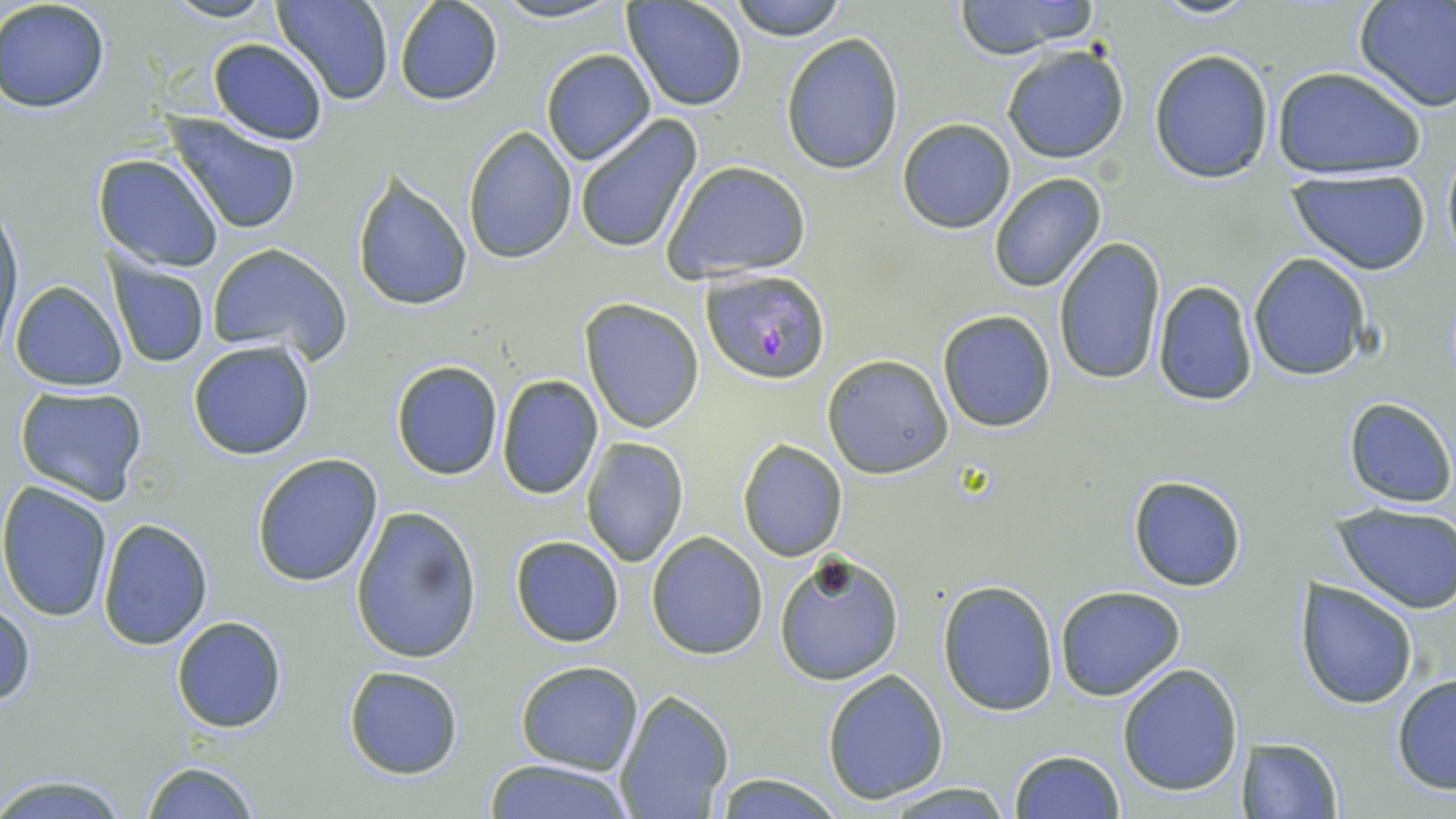
slide-level diagnosis = Plasmodium falciparum
uninfected red blood cell locations = approximate bounding boxes as [x1, y1, x2, y2] in pixels: [159, 0, 283, 24], [275, 0, 393, 106], [487, 0, 628, 24], [622, 0, 749, 112], [727, 0, 847, 41], [951, 0, 1105, 56], [1150, 0, 1258, 20], [1354, 0, 1456, 113], [0, 1, 112, 114], [392, 2, 502, 107], [781, 32, 905, 176], [206, 37, 329, 145], [999, 43, 1131, 166], [540, 49, 656, 165], [1148, 49, 1275, 182], [1271, 65, 1429, 179], [166, 114, 303, 235], [573, 115, 703, 254], [896, 118, 1016, 234], [462, 127, 577, 263], [1440, 153, 1456, 266], [93, 155, 223, 272], [659, 160, 811, 283], [1285, 170, 1433, 275], [350, 173, 473, 311], [988, 174, 1107, 293], [0, 202, 24, 347], [1053, 238, 1166, 386], [207, 242, 352, 364], [1248, 254, 1371, 381], [110, 260, 210, 369], [9, 280, 127, 390], [1151, 281, 1259, 406], [579, 298, 705, 434], [937, 311, 1056, 432], [187, 339, 316, 461], [821, 353, 954, 478], [390, 359, 503, 479], [496, 373, 603, 500], [13, 385, 149, 505], [1342, 397, 1454, 508], [581, 438, 689, 568], [737, 438, 848, 559], [251, 453, 383, 588], [1128, 473, 1249, 592], [0, 483, 113, 623], [1332, 502, 1456, 612], [349, 505, 482, 665], [97, 519, 213, 649], [647, 532, 767, 660], [509, 535, 625, 647], [774, 550, 904, 685], [937, 580, 1060, 716], [1296, 581, 1417, 707], [1055, 585, 1185, 700], [1, 600, 34, 708], [171, 616, 286, 733], [514, 660, 644, 776], [1117, 663, 1243, 796], [343, 665, 464, 780], [821, 671, 950, 804], [1390, 674, 1456, 795], [614, 690, 733, 819], [1240, 736, 1343, 817], [1010, 749, 1124, 818], [481, 759, 638, 818], [138, 760, 261, 819], [0, 772, 131, 817], [708, 772, 848, 817], [875, 781, 1018, 818]
stain = May-Grünwald-Giemsa
modality = optical microscopy
image size = 1456×819 pixels
Plasmodium falciparum-infected red blood cell locations = approximate bounding boxes as [x1, y1, x2, y2] in pixels: [701, 268, 832, 385]
preparation = thin blood smear
field of view = one of a larger specimen
magnification = 1000x